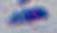

Summary:
  - Identification: Toxoplasma gondii
  - Modality: photomicrograph
  - Magnification: 1000x